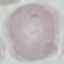
Summary:
  - Malaria status: uninfected
  - Stain: Giemsa
  - Capture: smartphone camera at the microscope eyepiece
  - Image type: cell patch, automatically extracted from a larger field of view and resized to 64 × 64 pixels
  - Preparation: thin blood smear